Describe the morphology of the red blood cells.
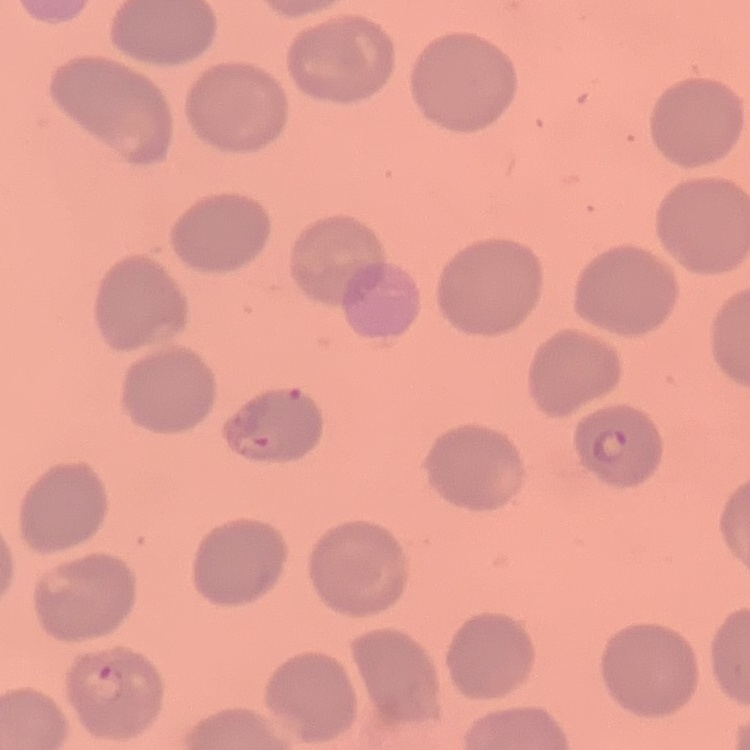

They show no rouleaux formation.

image type = square crop of a larger photomicrograph
preparation = thin blood smear
stain = Field's or Giemsa